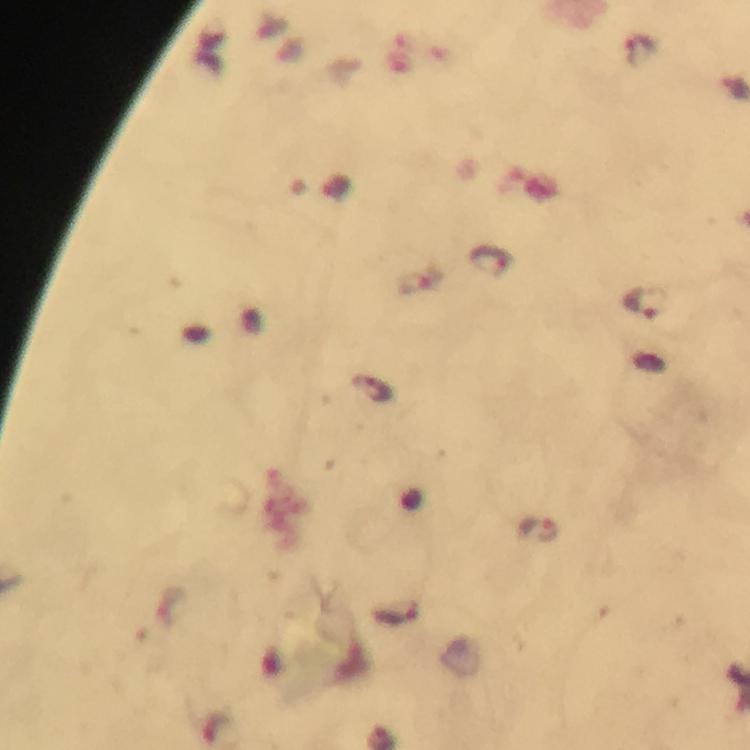

Approximate centers as (x, y) in pixels.
Summary:
  - Plasmodium parasite locations: (491, 260), (643, 303), (372, 388), (538, 530)
  - Image size: 750×750 pixels
  - Preparation: thick blood smear
  - Cropped from: one field of view
  - Immersion oil: used
  - Capture: smartphone mounted on the microscope
  - Magnification: 100x
  - Context: from a diagnostic examination for malaria
  - Stain: Giemsa